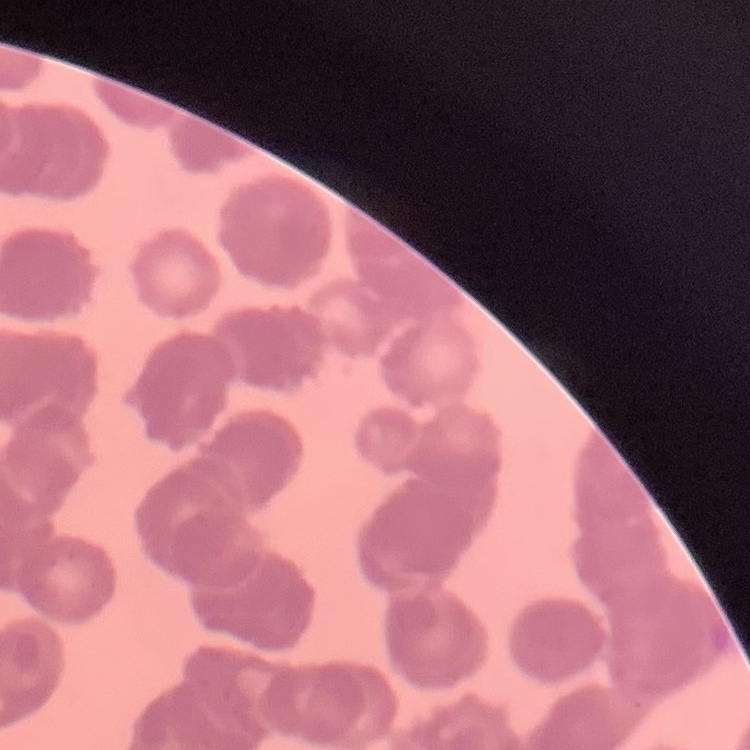
Summary:
  - Red blood cell morphology: rouleaux formation
  - Preparation: thin peripheral smear
  - Image type: square crop of a larger photomicrograph
  - Stain: Field's or Giemsa